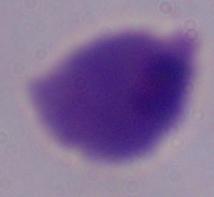
Summary:
  - Identification: trichomonad
  - Magnification: 1000x
  - Modality: photomicrograph